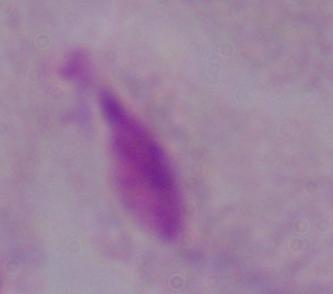
{
  "identification": "trichomonad",
  "magnification": "1000x",
  "modality": "photomicrograph"
}